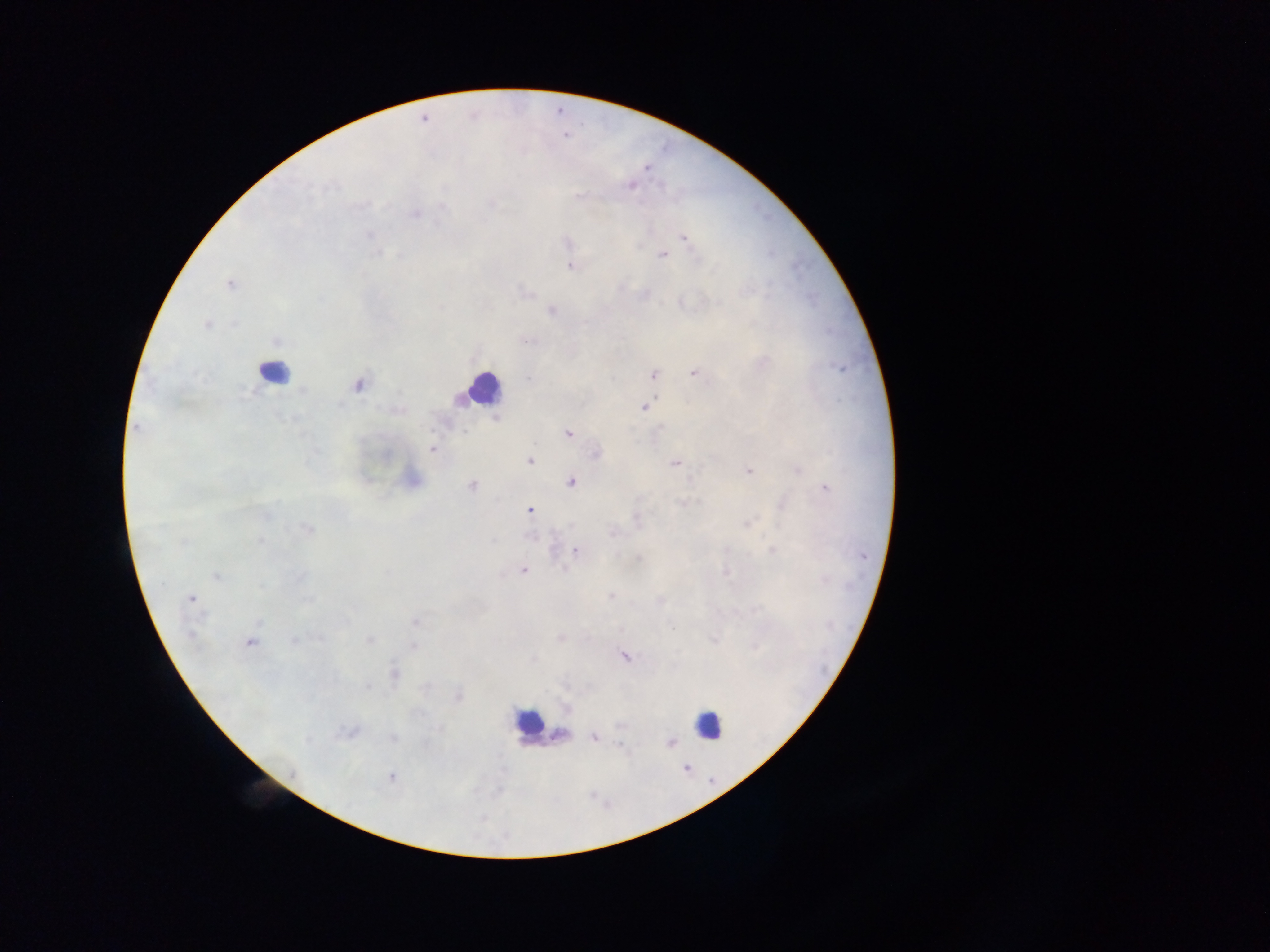

capture: mobile-phone photograph through a microscope
malaria_parasite_locations: 'approximate centers as x y in pixels: 646 167; 630 185; 578 196; 442 207; 415 214; 370 235; 684 238; 567 243; 378 252; 663 255; 570 267; 230 285; 551 310; 207 325; 277 341; 526 341; 763 362; 695 373; 654 374; 529 379; 358 385; 644 406; 137 428; 662 428; 568 433; 432 449; 596 454; 529 461; 675 463; 797 469; 748 471; 570 482; 472 486; 825 488; 682 503; 530 510; 265 516; 636 519; 748 524; 307 529; 613 532; 260 541; 493 541; 575 550; 726 550; 772 550; 638 558; 523 571; 726 572; 217 576; 300 577; 824 579; 163 585; 261 586; 610 596; 191 599; 660 602; 415 621; 259 622; 672 627; 190 635; 560 637; 320 639; 294 640; 370 640; 714 640; 250 642; 414 646; 754 647; 623 655; 533 660; 395 674; 367 688; 458 697; 619 725; 440 729; 348 732; 560 734; 594 737; 392 738; 308 740; 670 743; 622 747; 687 767; 293 772; 391 777'
leukocyte_locations: 'approximate centers as x y in pixels: 272 372; 481 389; 529 722; 709 724'
image_size: 1270×952 pixels
preparation: thick blood smear
field_of_view: single
country: Ghana